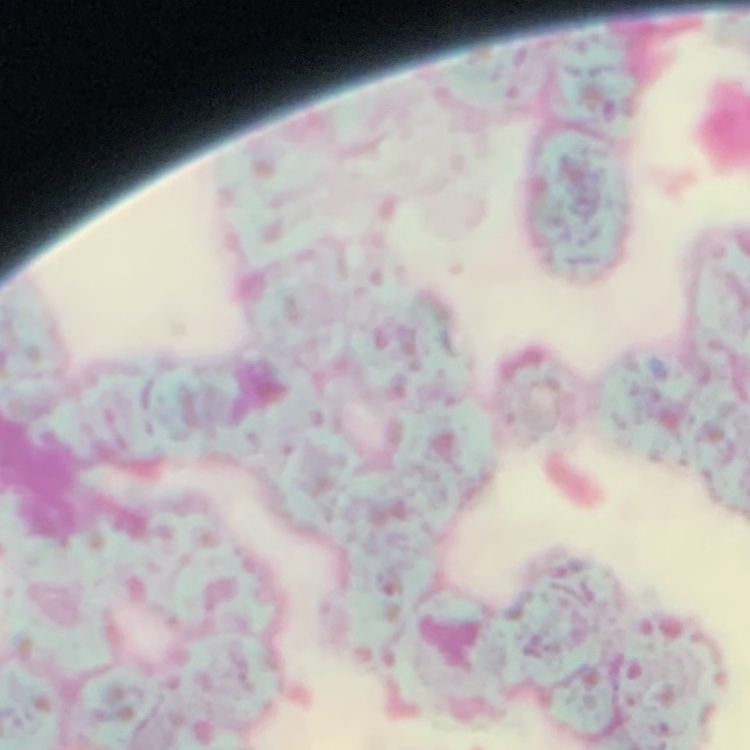
Summary:
  - Erythrocyte morphology: rouleaux formation
  - Image type: square crop of a larger photomicrograph
  - Preparation: thin blood film
  - Stain: Field's or Giemsa